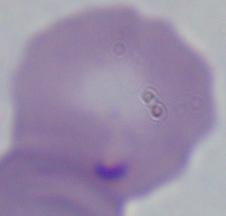
modality = photomicrograph
identification = Babesia
magnification = 1000x